Assess this cell for malaria.
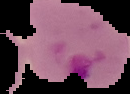

Parasitized.

Image is 130×94 pixels. From a thin blood smear. The area outside the segmented cell region is set to black.